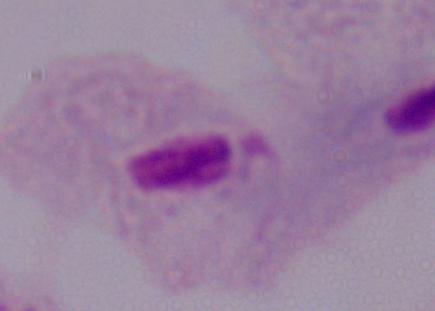

Summary:
  - Modality: micrograph
  - Magnification: 1000x
  - Identification: trichomonad